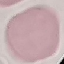

Summary:
  - Malaria status: uninfected
  - Preparation: thin blood film
  - Image type: automatically extracted cell patch, resized to 64 × 64 pixels
  - Capture: smartphone through the microscope eyepiece
  - Stain: Giemsa